Locate every Plasmodium malariae-infected red blood cell.
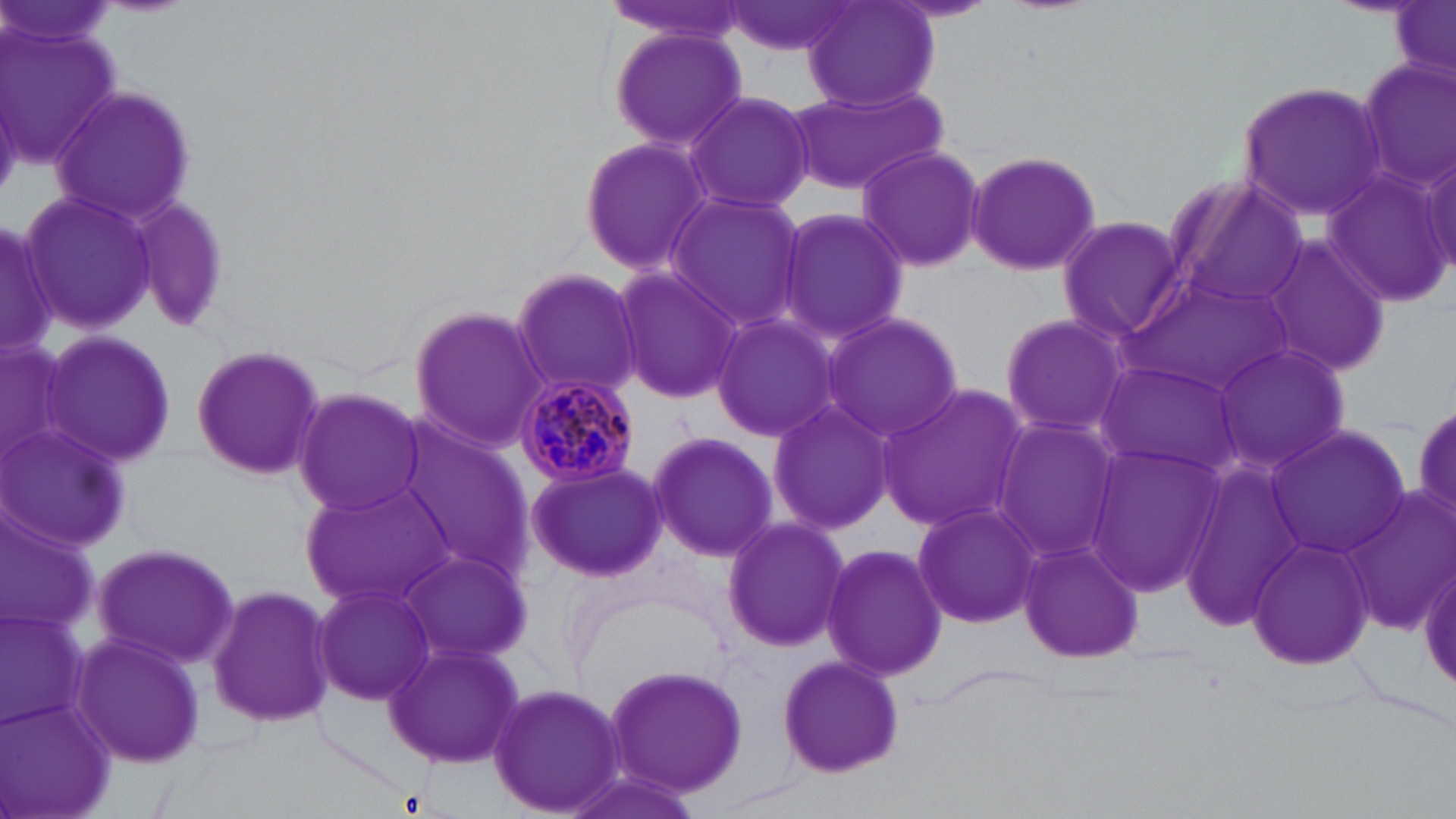

Approximate bounding boxes as (x1, y1, x2, y2) in pixels.
Plasmodium malariae-infected red blood cells: (513, 372, 641, 485).

Summary:
  - Uninfected red blood cell locations: (723, 0, 859, 57), (800, 0, 940, 113), (1391, 2, 1455, 86), (0, 19, 127, 171), (608, 25, 747, 154), (1355, 56, 1455, 199), (787, 79, 952, 199), (1239, 81, 1391, 219), (50, 83, 197, 226), (684, 91, 813, 214), (578, 136, 712, 272), (855, 143, 987, 272), (1416, 145, 1455, 285), (965, 148, 1104, 276), (1327, 163, 1454, 304), (1162, 176, 1311, 316), (20, 191, 158, 335), (664, 192, 808, 329), (127, 193, 232, 336), (776, 205, 910, 346), (1056, 216, 1184, 340), (0, 218, 57, 359), (1260, 233, 1395, 378), (509, 266, 641, 399), (613, 266, 744, 406), (1123, 267, 1298, 399), (407, 302, 551, 452), (820, 310, 963, 444), (995, 313, 1132, 440), (709, 314, 842, 442), (40, 331, 179, 469), (1, 336, 80, 471), (1211, 340, 1352, 475), (190, 342, 328, 482), (1093, 358, 1246, 480), (874, 382, 1030, 534), (292, 386, 426, 517), (766, 395, 892, 538), (1411, 395, 1456, 529), (989, 416, 1124, 565), (0, 424, 130, 552), (1264, 425, 1409, 561), (396, 426, 532, 577), (646, 429, 777, 561), (1084, 443, 1225, 592), (523, 461, 669, 582), (1178, 461, 1306, 626), (299, 476, 458, 609), (1341, 487, 1454, 633), (909, 501, 1042, 630), (0, 516, 98, 638), (720, 516, 850, 652), (1246, 535, 1375, 669), (1016, 536, 1142, 666), (90, 541, 240, 669), (820, 541, 947, 683), (397, 547, 531, 668), (1418, 554, 1455, 705), (313, 580, 437, 704), (206, 584, 338, 728), (0, 608, 86, 727), (70, 632, 206, 767), (384, 641, 522, 769), (774, 653, 905, 778), (603, 661, 752, 797), (487, 681, 628, 818), (0, 701, 116, 819), (559, 768, 703, 819)
  - Slide-level diagnosis: Plasmodium malariae
  - Stain: May-Grünwald-Giemsa
  - Field of view: one of a larger specimen
  - Image size: 1456×819 pixels
  - Modality: light microscopy
  - Preparation: thin blood film
  - Magnification: 1000x